Classify this cell by malaria status.
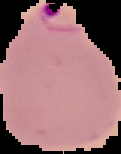
Parasitized.

preparation: thin blood film
image_size: 121×154 pixels
image_type: segmented cell region with the area outside set to black